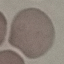
Summary:
  - Malaria status: uninfected
  - Image type: cell patch, automatically extracted from a larger field of view and resized to 64 × 64 pixels
  - Stain: Giemsa
  - Preparation: thin blood smear
  - Capture: smartphone through the microscope eyepiece